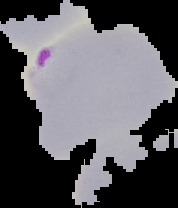

malaria status = parasitized
preparation = thin blood smear
image type = cell region segmented out of the field of view; surrounding area masked to black
image size = 178×208 pixels